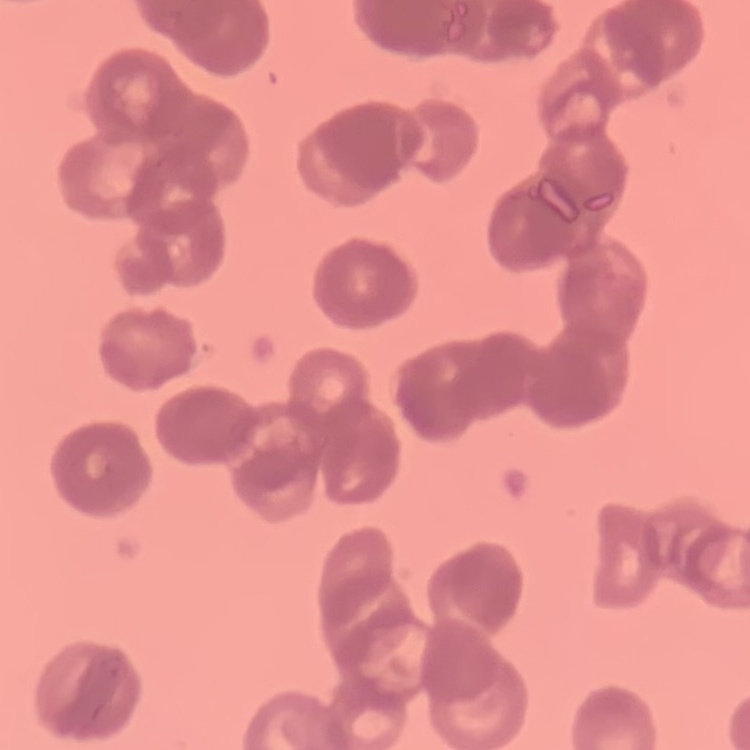

erythrocyte morphology = rouleaux formation
image type = square crop of a larger photomicrograph
stain = Field's or Giemsa
preparation = thin peripheral smear